Report the malaria status of this cell.
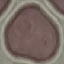

Uninfected.

image type = cell patch, automatically extracted from a larger field of view and resized to 64 × 64 pixels
preparation = thin smear
capture = smartphone through the microscope eyepiece
stain = Giemsa